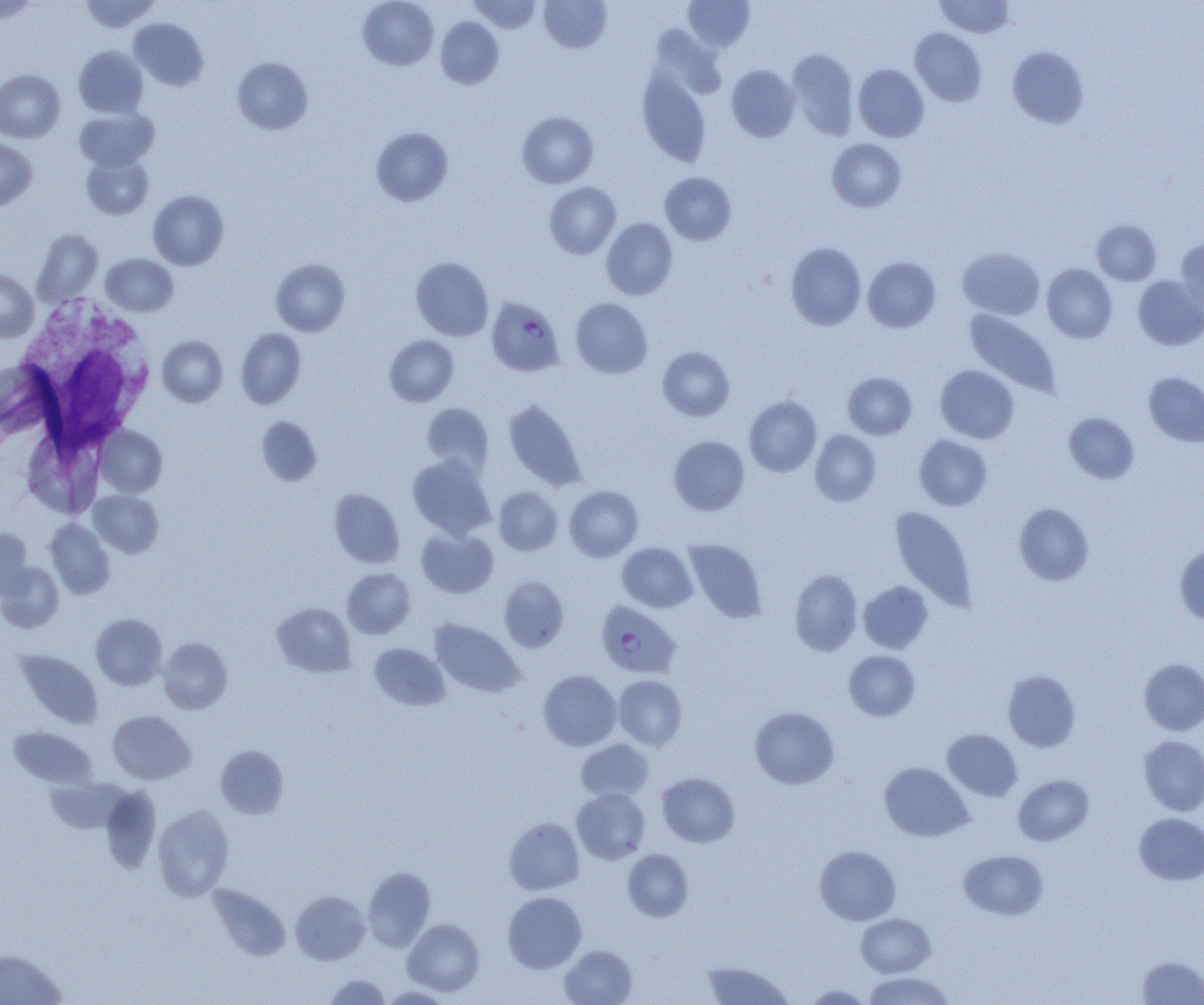

Approximate bounding boxes as named x1/y1/x2/y2 corners in pixels. Plasmodium falciparum-infected red blood cell locations: (x1=486, y1=297, x2=564, y2=376), (x1=596, y1=601, x2=681, y2=679). Uninfected red blood cell locations: (x1=79, y1=0, x2=160, y2=33), (x1=358, y1=0, x2=438, y2=70), (x1=469, y1=0, x2=542, y2=33), (x1=539, y1=0, x2=611, y2=52), (x1=683, y1=0, x2=755, y2=51), (x1=935, y1=0, x2=1016, y2=38), (x1=0, y1=1, x2=39, y2=23), (x1=435, y1=17, x2=504, y2=89), (x1=129, y1=18, x2=209, y2=90), (x1=910, y1=28, x2=987, y2=106), (x1=74, y1=46, x2=148, y2=117), (x1=1008, y1=46, x2=1089, y2=128), (x1=787, y1=49, x2=859, y2=140), (x1=232, y1=57, x2=313, y2=134), (x1=853, y1=64, x2=929, y2=142), (x1=726, y1=65, x2=800, y2=142), (x1=637, y1=68, x2=711, y2=166), (x1=0, y1=69, x2=64, y2=143), (x1=75, y1=108, x2=158, y2=171), (x1=517, y1=111, x2=598, y2=188), (x1=371, y1=126, x2=453, y2=206), (x1=827, y1=138, x2=906, y2=212), (x1=0, y1=139, x2=37, y2=210), (x1=82, y1=153, x2=153, y2=219), (x1=659, y1=172, x2=736, y2=245), (x1=544, y1=182, x2=621, y2=258), (x1=148, y1=190, x2=229, y2=270), (x1=601, y1=217, x2=678, y2=300), (x1=1092, y1=219, x2=1161, y2=285), (x1=32, y1=229, x2=102, y2=306), (x1=1175, y1=239, x2=1204, y2=318), (x1=785, y1=242, x2=866, y2=330), (x1=957, y1=246, x2=1045, y2=320), (x1=102, y1=253, x2=178, y2=316), (x1=411, y1=257, x2=494, y2=341), (x1=863, y1=257, x2=940, y2=332), (x1=271, y1=258, x2=350, y2=336), (x1=1042, y1=264, x2=1117, y2=342), (x1=0, y1=270, x2=38, y2=341), (x1=1133, y1=276, x2=1204, y2=350), (x1=570, y1=298, x2=653, y2=378), (x1=964, y1=309, x2=1061, y2=397), (x1=236, y1=328, x2=306, y2=408), (x1=157, y1=335, x2=228, y2=406), (x1=384, y1=335, x2=459, y2=406), (x1=657, y1=346, x2=734, y2=421), (x1=936, y1=365, x2=1019, y2=443), (x1=843, y1=372, x2=917, y2=439), (x1=1144, y1=372, x2=1204, y2=446), (x1=744, y1=396, x2=822, y2=477), (x1=504, y1=400, x2=586, y2=490), (x1=421, y1=402, x2=494, y2=475), (x1=1063, y1=412, x2=1140, y2=483), (x1=257, y1=416, x2=322, y2=486), (x1=96, y1=425, x2=167, y2=496), (x1=810, y1=430, x2=881, y2=506), (x1=914, y1=435, x2=992, y2=511), (x1=668, y1=436, x2=750, y2=515), (x1=32, y1=441, x2=98, y2=514), (x1=407, y1=455, x2=496, y2=540), (x1=493, y1=486, x2=563, y2=555), (x1=565, y1=486, x2=643, y2=561), (x1=329, y1=488, x2=404, y2=568), (x1=89, y1=490, x2=164, y2=557), (x1=1014, y1=502, x2=1094, y2=585), (x1=890, y1=506, x2=977, y2=611), (x1=45, y1=519, x2=115, y2=599), (x1=0, y1=528, x2=33, y2=598), (x1=416, y1=528, x2=499, y2=598), (x1=685, y1=539, x2=767, y2=622), (x1=617, y1=542, x2=697, y2=612), (x1=1175, y1=544, x2=1204, y2=626), (x1=0, y1=561, x2=64, y2=633), (x1=342, y1=567, x2=415, y2=639), (x1=789, y1=569, x2=862, y2=655), (x1=499, y1=577, x2=569, y2=652), (x1=858, y1=581, x2=933, y2=653), (x1=272, y1=602, x2=356, y2=677), (x1=90, y1=614, x2=167, y2=690), (x1=429, y1=619, x2=524, y2=697), (x1=158, y1=637, x2=232, y2=714), (x1=369, y1=643, x2=450, y2=710), (x1=15, y1=650, x2=103, y2=728), (x1=844, y1=650, x2=920, y2=721), (x1=1139, y1=658, x2=1204, y2=736), (x1=538, y1=670, x2=621, y2=751), (x1=1002, y1=670, x2=1081, y2=752), (x1=613, y1=675, x2=687, y2=750), (x1=750, y1=706, x2=839, y2=789), (x1=107, y1=710, x2=196, y2=784), (x1=8, y1=726, x2=96, y2=788), (x1=942, y1=728, x2=1023, y2=801), (x1=1139, y1=736, x2=1204, y2=816), (x1=576, y1=739, x2=654, y2=802), (x1=215, y1=745, x2=289, y2=818), (x1=880, y1=762, x2=973, y2=841), (x1=656, y1=772, x2=740, y2=847), (x1=1013, y1=775, x2=1094, y2=846), (x1=100, y1=785, x2=161, y2=873), (x1=571, y1=787, x2=651, y2=864), (x1=153, y1=804, x2=234, y2=901), (x1=1134, y1=813, x2=1204, y2=885), (x1=504, y1=817, x2=584, y2=895), (x1=814, y1=845, x2=901, y2=925), (x1=622, y1=849, x2=694, y2=921), (x1=958, y1=849, x2=1049, y2=920), (x1=363, y1=867, x2=435, y2=951), (x1=207, y1=884, x2=290, y2=961), (x1=290, y1=890, x2=370, y2=965), (x1=502, y1=892, x2=586, y2=973), (x1=856, y1=913, x2=935, y2=977), (x1=402, y1=919, x2=484, y2=996), (x1=559, y1=945, x2=637, y2=1005), (x1=0, y1=948, x2=67, y2=1005), (x1=1137, y1=955, x2=1204, y2=1004), (x1=702, y1=960, x2=793, y2=1005), (x1=862, y1=971, x2=955, y2=1005), (x1=324, y1=974, x2=391, y2=1004), (x1=802, y1=984, x2=873, y2=1004), (x1=379, y1=986, x2=455, y2=1003). White blood cell locations: (x1=13, y1=297, x2=156, y2=454). Slide-level diagnosis: Plasmodium falciparum. One field of a larger specimen. Light microscopy. Image is 1204×1005 pixels. Captured at 1000x magnification. Thin blood film.